Assess this cell for malaria.
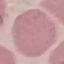

Uninfected.

Summary:
  - Stain: Giemsa
  - Image type: cell patch, automatically extracted from a larger field of view and resized to 64 × 64 pixels
  - Preparation: thin blood smear
  - Capture: smartphone through the microscope eyepiece